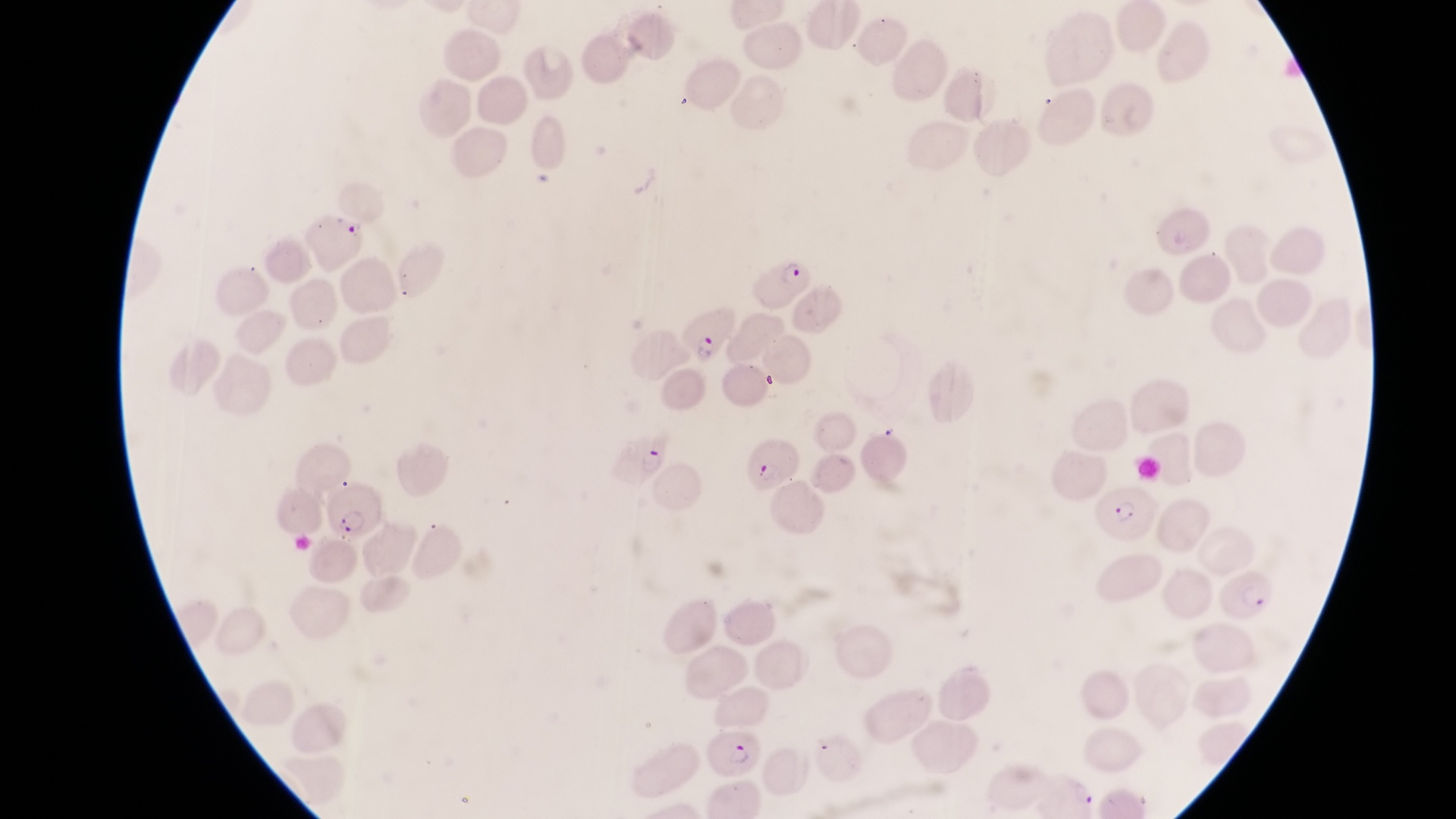
preparation = thin blood film
field of view = single
image size = 1456×819 pixels
capture = smartphone photograph through the eyepiece of an Olympus CX-23 microscope
magnification = 1000x
country = Uganda
parasitised red blood cell locations = approximate bounding boxes as (left, top, right, bottom) in pixels: (298, 206, 372, 266), (750, 253, 811, 311), (668, 296, 735, 363), (607, 430, 674, 490), (748, 439, 807, 495), (323, 485, 383, 540), (1089, 485, 1156, 541), (1213, 561, 1272, 624), (704, 727, 763, 777)